Describe the morphology of the erythrocytes.
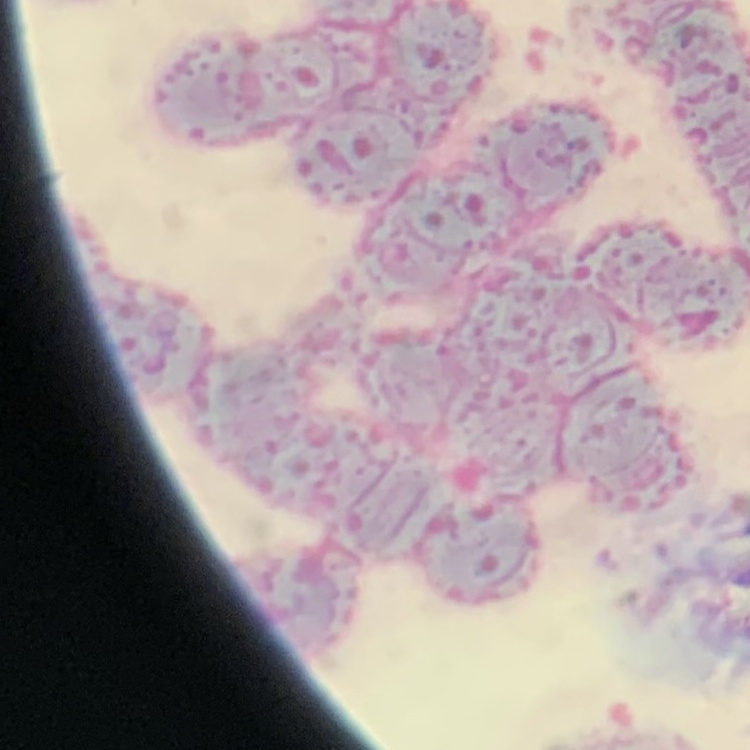
They show rouleaux formation.

stain = Field's or Giemsa
image type = square crop of a larger photomicrograph
preparation = thin blood film